Point out each malaria parasite.
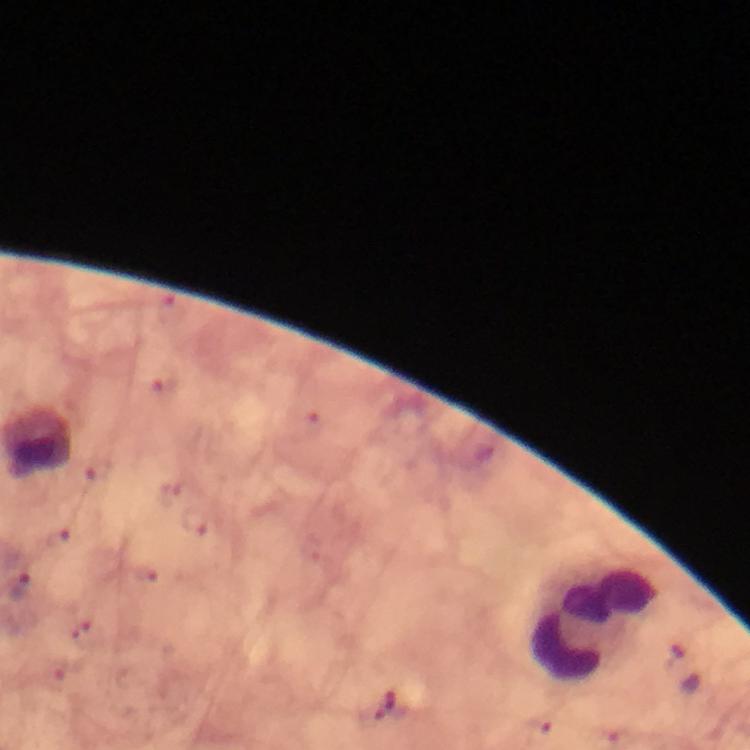

Approximate object centers, in pixels from the top-left corner.
Malaria parasites: (x=20, y=589).

Leukocyte locations: (x=594, y=622). From a malaria diagnostic workup. Image is 750×750 pixels. A crop from one field of view. Thick smear. At 100x magnification. Giemsa-stained preparation. Immersion oil applied. Photographed with a smartphone mounted on the microscope.